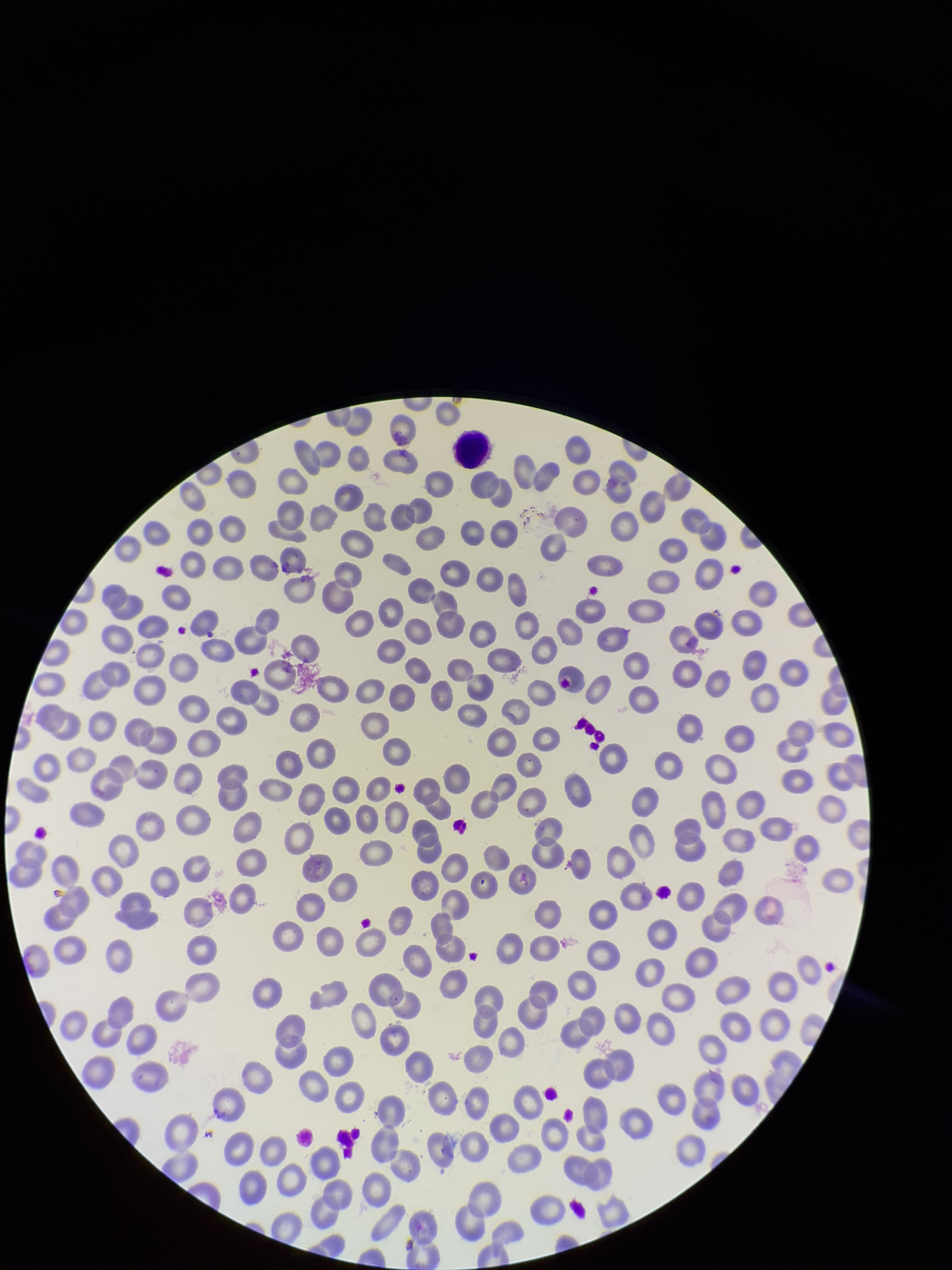

Parasitized red blood cells: none seen. Patient malaria status: negative. Red blood cell count: 290. Single field of view. Parasitized red blood cell count: 0. Preparation: thin blood smear. Smartphone photograph taken through the eyepiece of a microscope. Image is 952×1270 pixels. Stained with Giemsa.